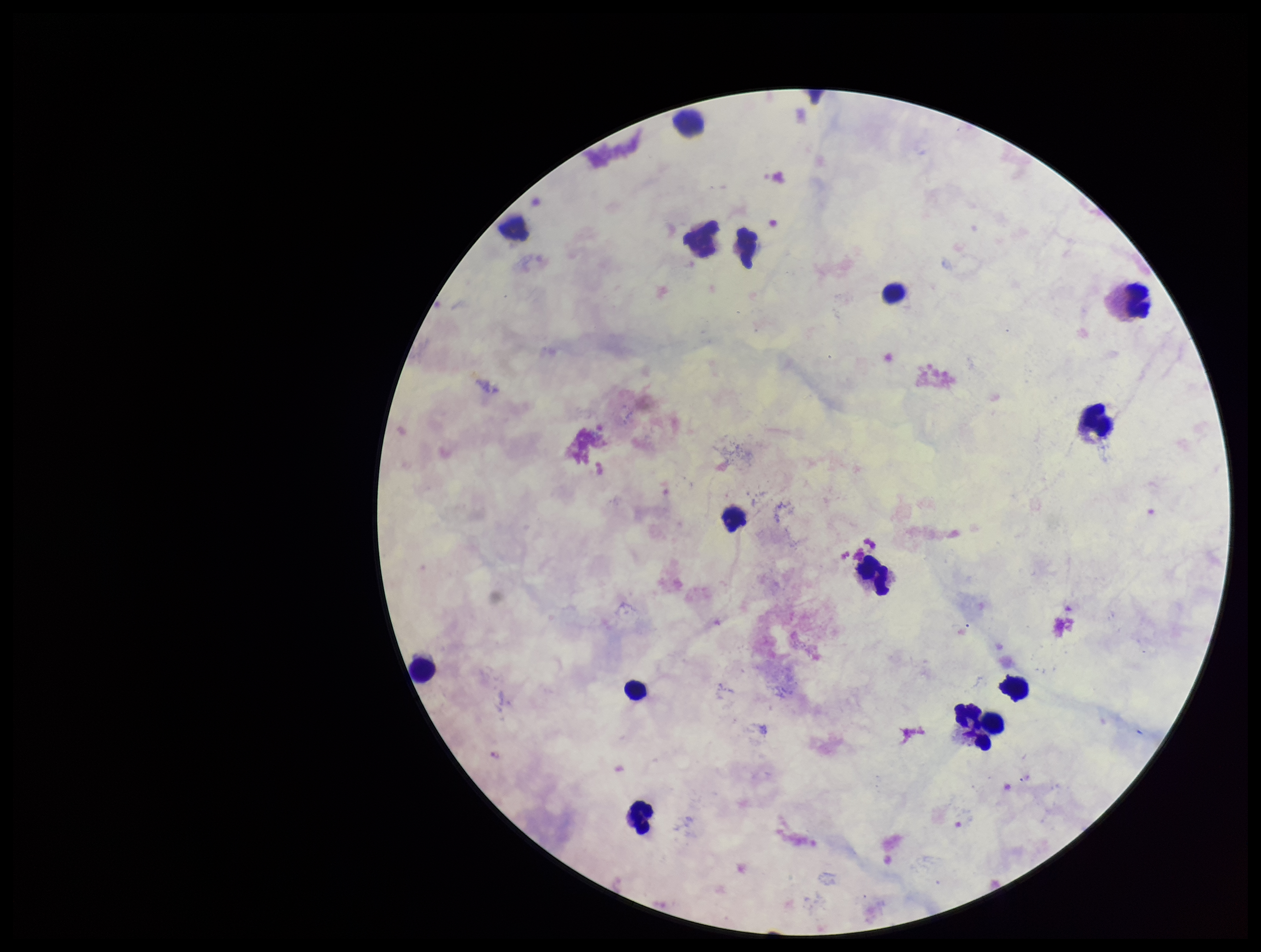
Summary:
  - Preparation: thick
  - Patient malaria status: negative
  - Plasmodium parasites: none seen
  - Stain: Giemsa
  - Leukocyte count: 14
  - Parasite count: 0
  - Image size: 1261×952 pixels
  - Field of view: one from this slide
  - Capture: smartphone photograph through the microscope eyepiece